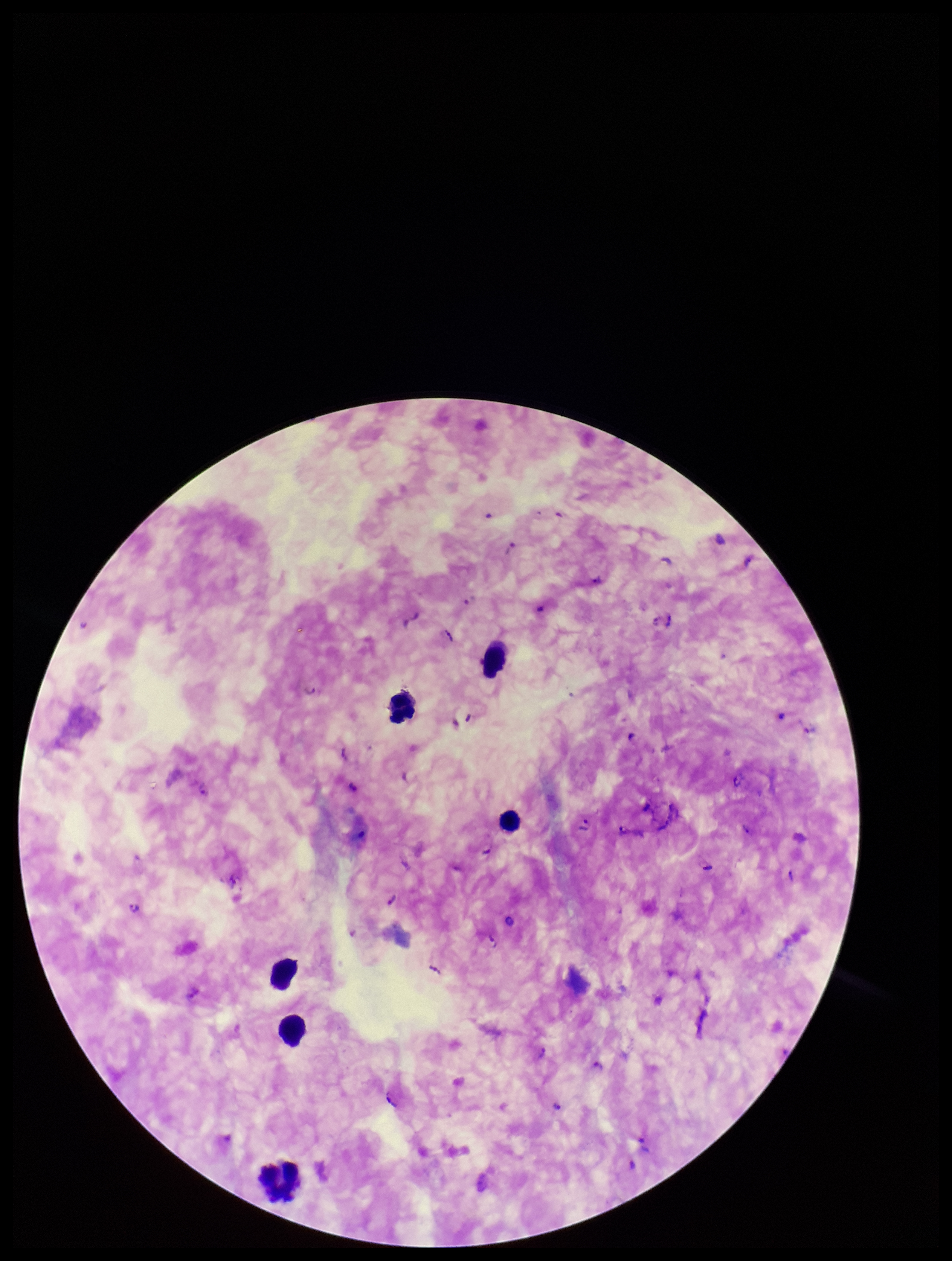

Summary:
  - Image size: 952×1261 pixels
  - Plasmodium parasites: seen
  - Field of view: single
  - Capture: smartphone photograph through the microscope eyepiece
  - Stain: Giemsa
  - Parasite count: 30
  - Leukocyte count: 6
  - Species reported for this patient: Plasmodium falciparum
  - Preparation: thick
  - Patient malaria status: infected